Comment on the morphology of the erythrocytes.
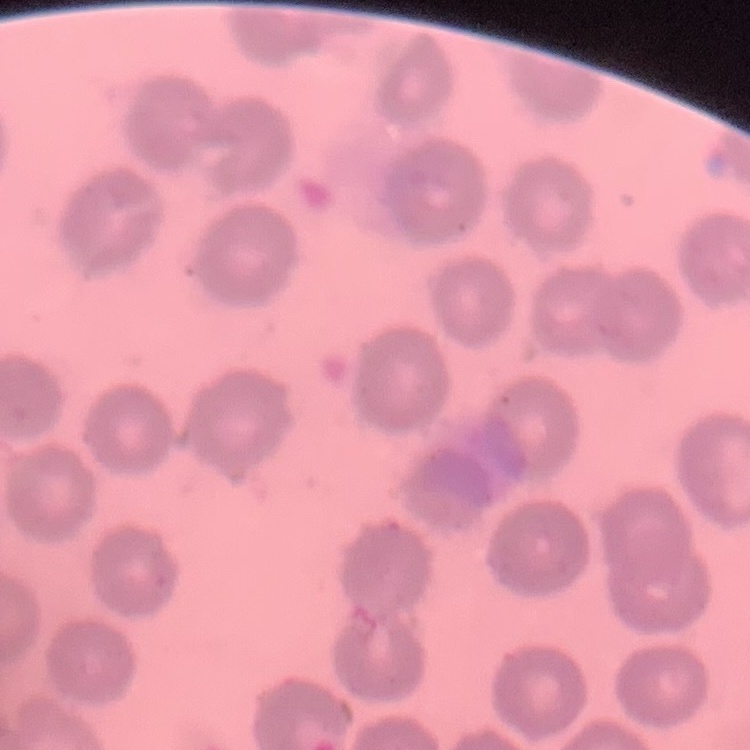

They show no rouleaux formation.

preparation = thin blood smear
stain = Field's or Giemsa
image type = square crop of a larger photomicrograph